Report the malaria status of this cell.
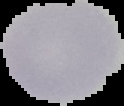
It is uninfected.

Summary:
  - Image type: segmented cell region on a black background
  - Preparation: thin blood film
  - Image size: 124×106 pixels